Classify this cell by malaria status.
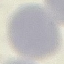
Uninfected.

Cell patch, automatically extracted from a larger field of view and resized to 64 × 64 pixels. Acquired by smartphone through the microscope eyepiece. Giemsa stain. Thin blood film.